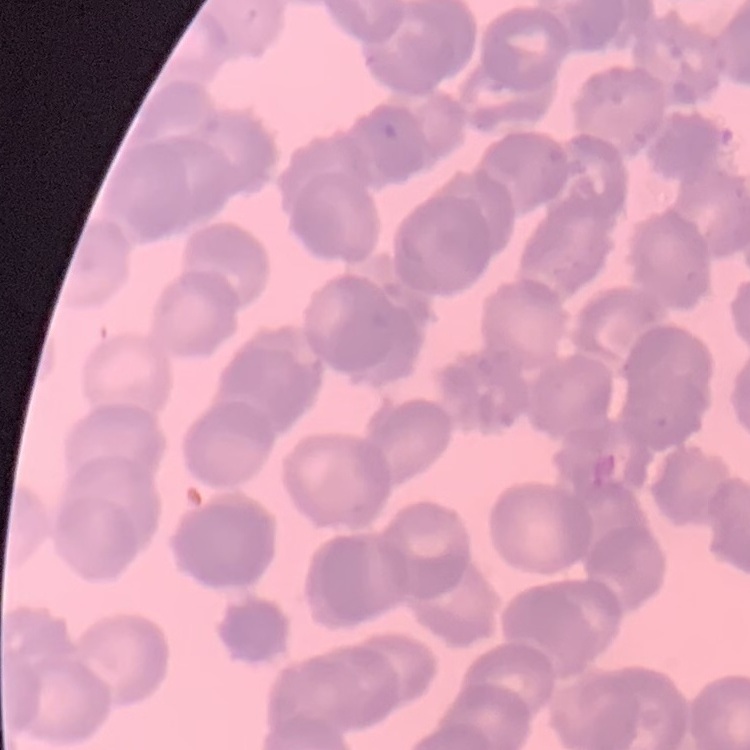

erythrocyte morphology = rouleaux formation
image type = one tile cut from a larger photomicrograph
preparation = thin blood film
stain = Field's or Giemsa